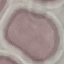
Malaria status: uninfected. Giemsa-stained preparation. Photographed with a smartphone camera at the microscope eyepiece. Thin smear of blood. Cell patch, automatically extracted from a larger field of view and resized to 64 × 64 pixels.